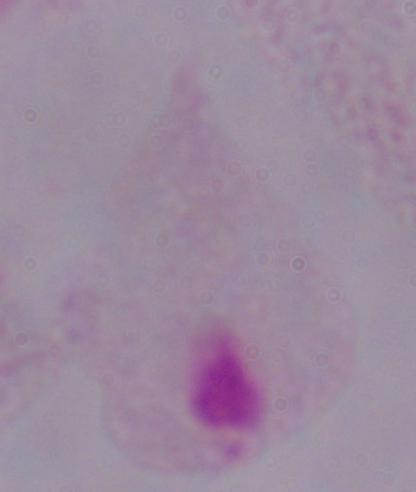
Summary:
  - Modality: photomicrograph
  - Identification: trichomonad
  - Magnification: 1000x